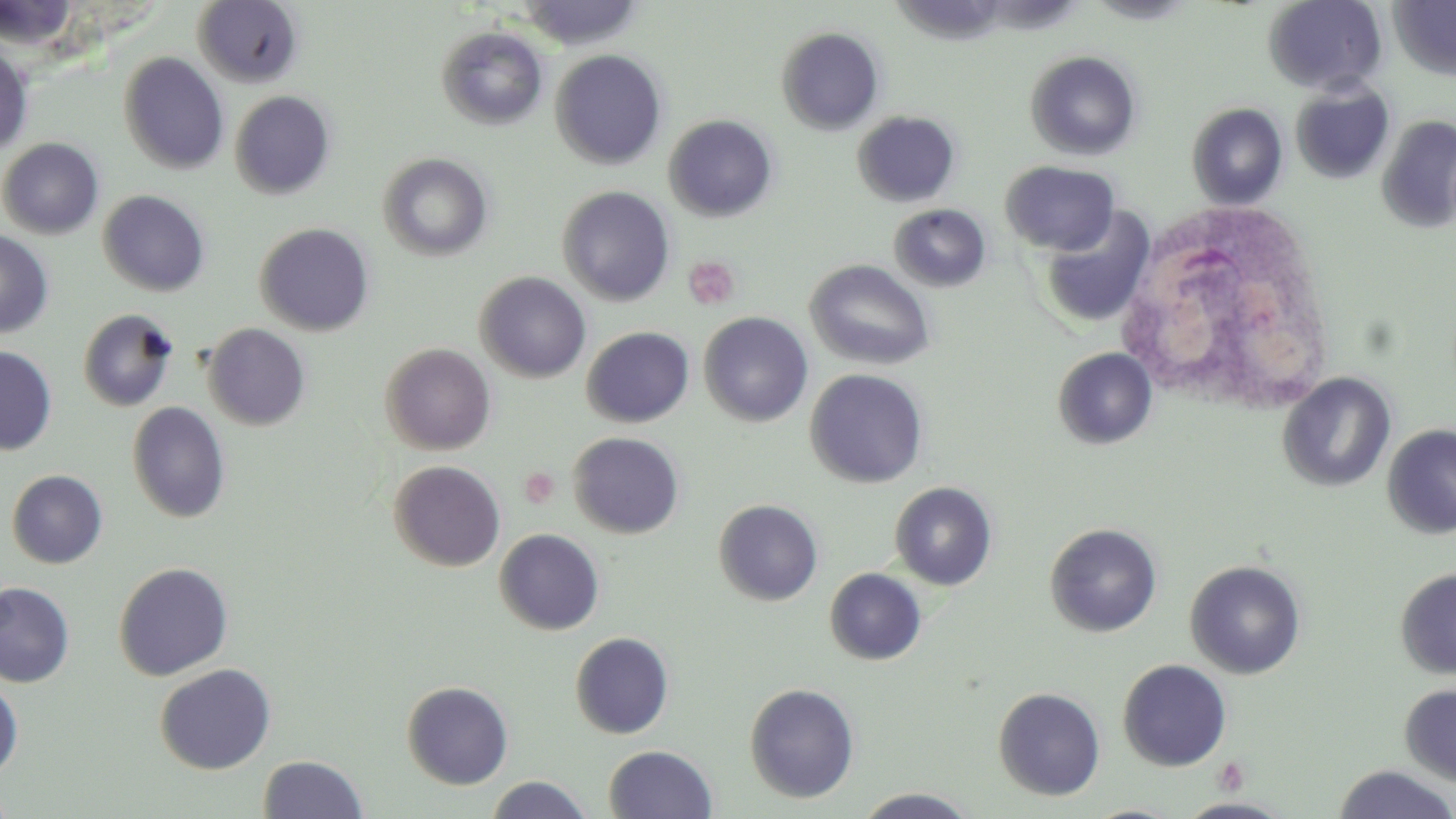
Approximate bounding boxes as (x1,y1)-(x2,y2) corner pairs in pixels. Uninfected red blood cell locations: (1085,0)-(1201,24), (1263,0)-(1387,95), (1388,0)-(1456,80), (192,1)-(304,87), (437,25)-(548,130), (775,26)-(885,135), (0,42)-(33,158), (550,49)-(667,170), (1025,50)-(1142,161), (118,52)-(230,174), (1291,81)-(1395,184), (230,90)-(335,200), (1187,102)-(1288,210), (852,110)-(961,208), (664,114)-(778,222), (1376,115)-(1456,233), (0,138)-(104,239), (378,152)-(494,261), (1001,160)-(1120,256), (557,185)-(675,306), (98,189)-(210,296), (889,203)-(991,293), (1039,207)-(1156,328), (255,222)-(375,336), (0,228)-(54,338), (805,259)-(936,370), (475,272)-(591,383), (77,308)-(180,412), (698,311)-(813,427), (203,323)-(311,431), (581,327)-(694,427), (380,342)-(496,455), (0,345)-(57,455), (1052,347)-(1157,449), (805,368)-(929,488), (1277,372)-(1396,493), (127,401)-(230,523), (1382,424)-(1456,540), (568,432)-(685,539), (388,460)-(506,572), (6,469)-(108,569), (890,481)-(998,590), (714,499)-(823,606), (1044,522)-(1162,637), (494,528)-(605,636), (1184,560)-(1306,680), (113,561)-(233,680), (824,567)-(927,665), (1395,567)-(1456,679), (0,581)-(75,688), (569,632)-(675,739), (1118,659)-(1232,771), (154,663)-(276,774), (0,680)-(24,778), (401,680)-(513,789), (744,682)-(860,803), (1399,684)-(1456,786), (993,687)-(1105,800), (603,745)-(717,819), (258,754)-(367,818), (1332,764)-(1456,819), (484,775)-(594,818), (0,784)-(16,818), (852,787)-(981,818), (1177,798)-(1292,818). White blood cell locations: (1114,200)-(1338,418). Platelet locations: (684,256)-(740,310), (520,467)-(560,509), (1215,756)-(1250,795). Slide-level diagnosis: no evidence of blood parasites. Optical microscopy. Image is 1456×819 pixels. Thin blood film. May-Grünwald-Giemsa-stained preparation. 1000x magnification. One field of a larger specimen.